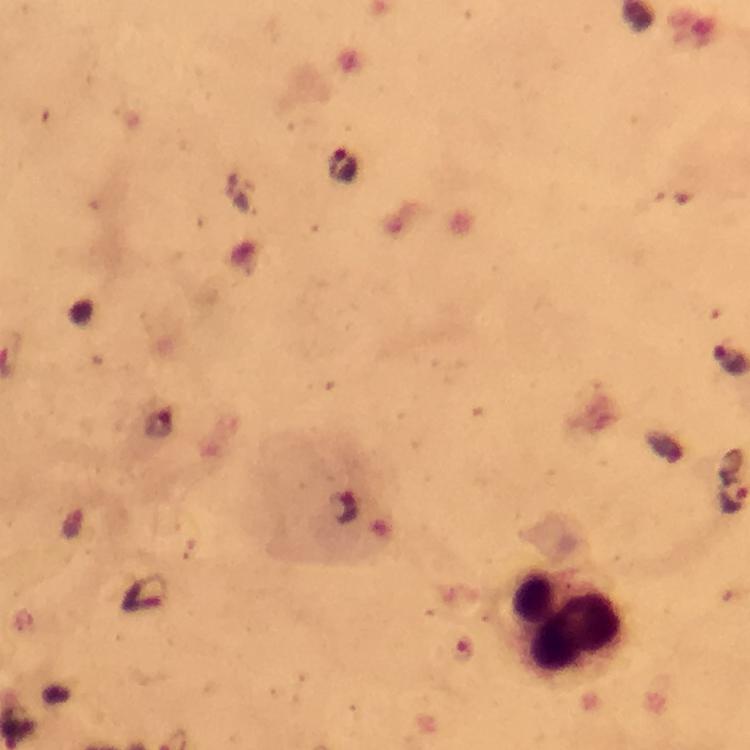
{
  "stain": "Giemsa",
  "cropped_from": "a single field of view",
  "capture": "smartphone mounted on the microscope",
  "plasmodium_parasite_locations": "approximate centers as (x, y) in pixels: (342, 165), (734, 500)",
  "immersion_oil": "used",
  "image_size": "750×750 pixels",
  "context": "from a diagnostic examination for malaria",
  "leukocyte_locations": "approximate centers as (x, y) in pixels: (568, 625)",
  "preparation": "thick smear",
  "magnification": "100x"
}